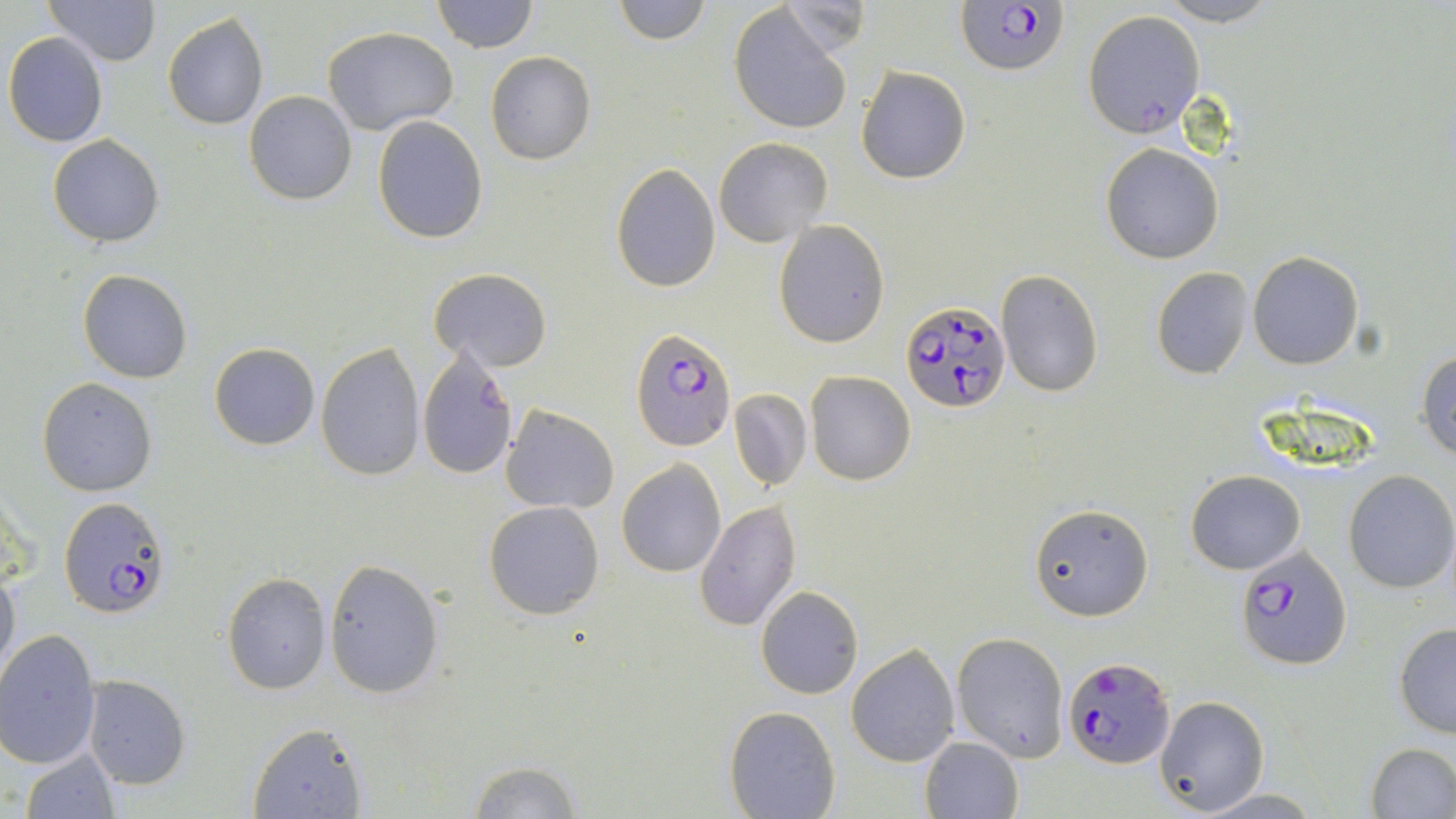
slide-level diagnosis = Plasmodium falciparum
field of view = one of a larger specimen
uninfected red blood cell locations = approximate bounding boxes as (x1,y1)-(x2,y2) corner pairs in pixels: (45,0)-(161,68), (431,0)-(539,54), (612,0)-(710,45), (777,1)-(870,60), (1155,1)-(1282,26), (729,4)-(854,134), (1082,10)-(1205,138), (162,12)-(268,130), (323,25)-(458,133), (3,32)-(110,148), (485,51)-(595,166), (856,65)-(972,185), (244,91)-(357,205), (372,115)-(488,243), (47,135)-(164,246), (714,138)-(833,247), (1100,143)-(1224,264), (610,163)-(721,291), (773,219)-(889,349), (1248,252)-(1364,369), (1152,266)-(1253,379), (430,268)-(552,371), (77,269)-(192,384), (997,271)-(1102,395), (316,343)-(425,481), (209,344)-(320,450), (416,347)-(518,479), (1418,351)-(1456,460), (805,370)-(916,486), (37,377)-(157,497), (730,389)-(811,490), (500,404)-(619,514), (617,459)-(725,576), (1342,470)-(1456,593), (1187,471)-(1306,574), (696,498)-(802,633), (483,500)-(606,620), (1029,503)-(1151,621), (323,560)-(446,698), (0,568)-(20,685), (223,573)-(331,694), (755,586)-(863,699), (1393,621)-(1456,738), (0,631)-(101,768), (951,632)-(1069,760), (847,645)-(960,766), (83,677)-(190,789), (1155,695)-(1268,815), (725,707)-(841,819), (248,723)-(367,818), (919,737)-(1024,819), (1366,742)-(1456,818), (19,747)-(120,818), (466,759)-(580,817), (1191,786)-(1323,817)
magnification = 1000x
Plasmodium falciparum-infected red blood cell locations = approximate bounding boxes as (x1,y1)-(x2,y2) corner pairs in pixels: (957,0)-(1069,77), (901,300)-(1010,412), (630,328)-(734,452), (62,498)-(171,618), (1238,546)-(1353,670), (1064,656)-(1175,770)
preparation = thin blood film
image size = 1456×819 pixels
stain = May-Grünwald-Giemsa
modality = optical microscopy